Name the parasite shown.
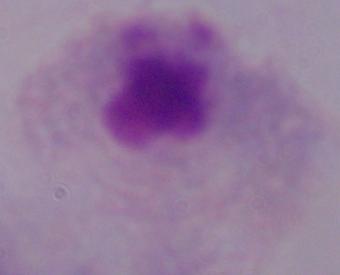

This is a trichomonad.

{
  "magnification": "1000x",
  "modality": "photomicrograph"
}